Locate and identify every blood parasite.
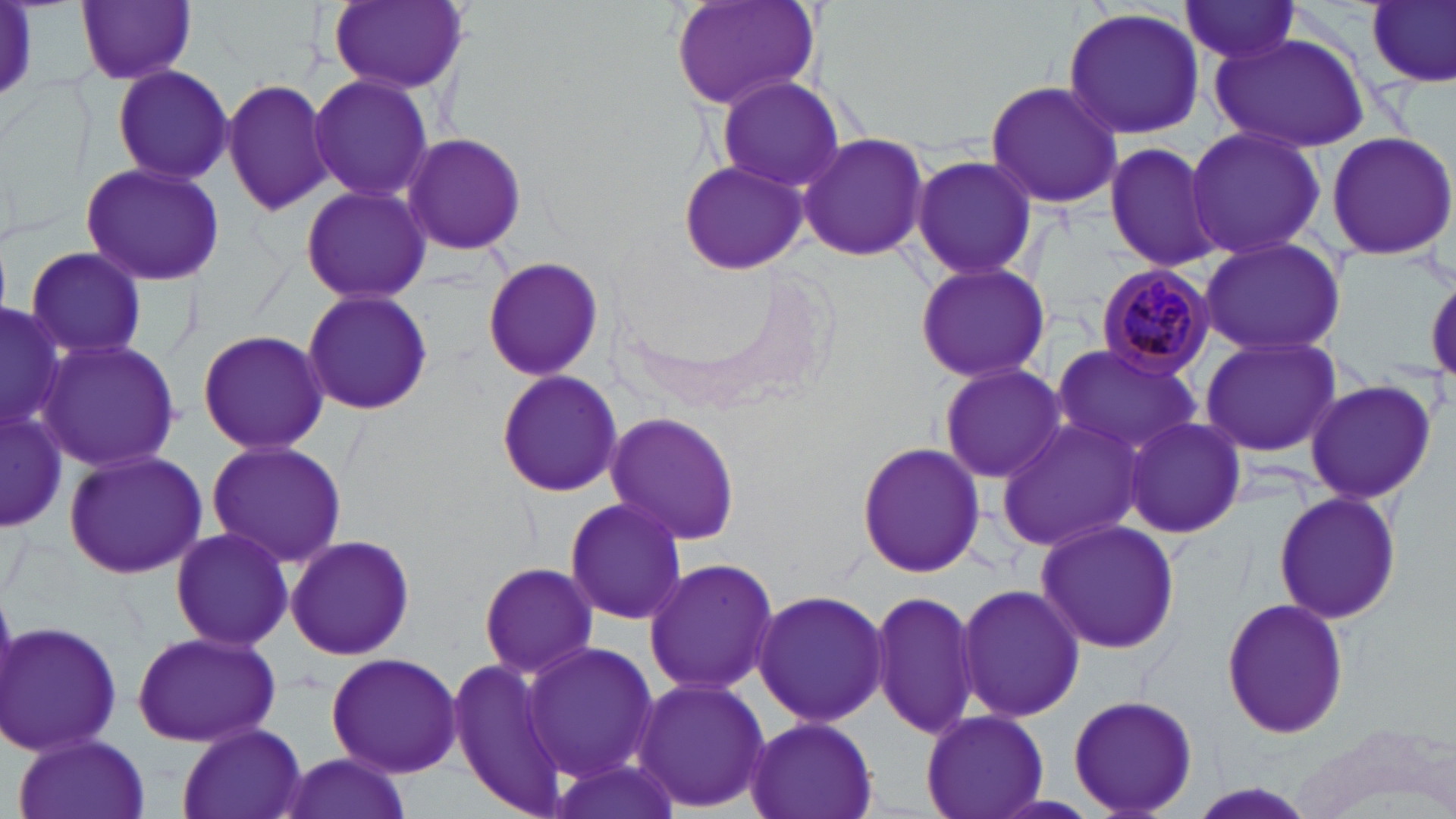

Approximate bounding boxes as (x1,y1)-(x2,y2) corner pairs in pixels.
Plasmodium malariae-infected red blood cells: (1091,261)-(1222,379).
No Plasmodium falciparum, Plasmodium ovale, Plasmodium vivax, Babesia divergens, or Trypanosoma brucei observed.

Summary:
  - Uninfected red blood cell locations: (76,0)-(197,86), (326,0)-(469,95), (666,0)-(825,114), (1366,0)-(1456,87), (1178,1)-(1306,66), (0,4)-(48,109), (1060,6)-(1208,139), (1210,30)-(1371,153), (112,64)-(234,186), (308,72)-(435,206), (714,75)-(846,194), (221,78)-(336,217), (984,80)-(1124,210), (1185,123)-(1325,260), (1323,130)-(1456,261), (401,131)-(527,255), (797,132)-(930,262), (1103,138)-(1223,273), (910,153)-(1037,283), (677,159)-(807,275), (78,161)-(227,285), (298,181)-(435,306), (1193,236)-(1351,359), (22,247)-(149,361), (482,256)-(606,383), (914,259)-(1050,384), (300,288)-(435,416), (0,301)-(67,437), (195,329)-(331,455), (1198,333)-(1343,460), (35,338)-(184,472), (1050,342)-(1206,459), (933,362)-(1069,485), (1060,362)-(1231,527), (494,369)-(625,500), (1305,377)-(1437,503), (1,408)-(68,533), (602,411)-(742,547), (1122,415)-(1246,540), (992,417)-(1146,554), (206,439)-(347,569), (855,441)-(986,579), (61,449)-(209,579), (1274,491)-(1402,623), (563,498)-(687,627), (1033,519)-(1181,655), (170,526)-(297,651), (284,534)-(416,661), (644,557)-(779,695), (478,560)-(597,679), (956,583)-(1085,723), (752,588)-(890,727), (871,589)-(980,741), (1220,597)-(1350,741), (2,620)-(123,760), (131,629)-(282,749), (521,641)-(661,782), (325,649)-(463,777), (445,660)-(570,810), (632,676)-(772,814), (1066,693)-(1199,817), (918,708)-(1047,819), (744,716)-(878,819), (176,723)-(308,819), (1296,723)-(1456,819), (11,730)-(154,819), (273,750)-(409,819), (543,751)-(684,819)
  - Slide-level diagnosis: Plasmodium malariae
  - Stain: May-Grünwald-Giemsa
  - Magnification: 1000x
  - Modality: optical microscopy
  - Image size: 1456×819 pixels
  - Field of view: one of a larger specimen
  - Preparation: thin blood smear